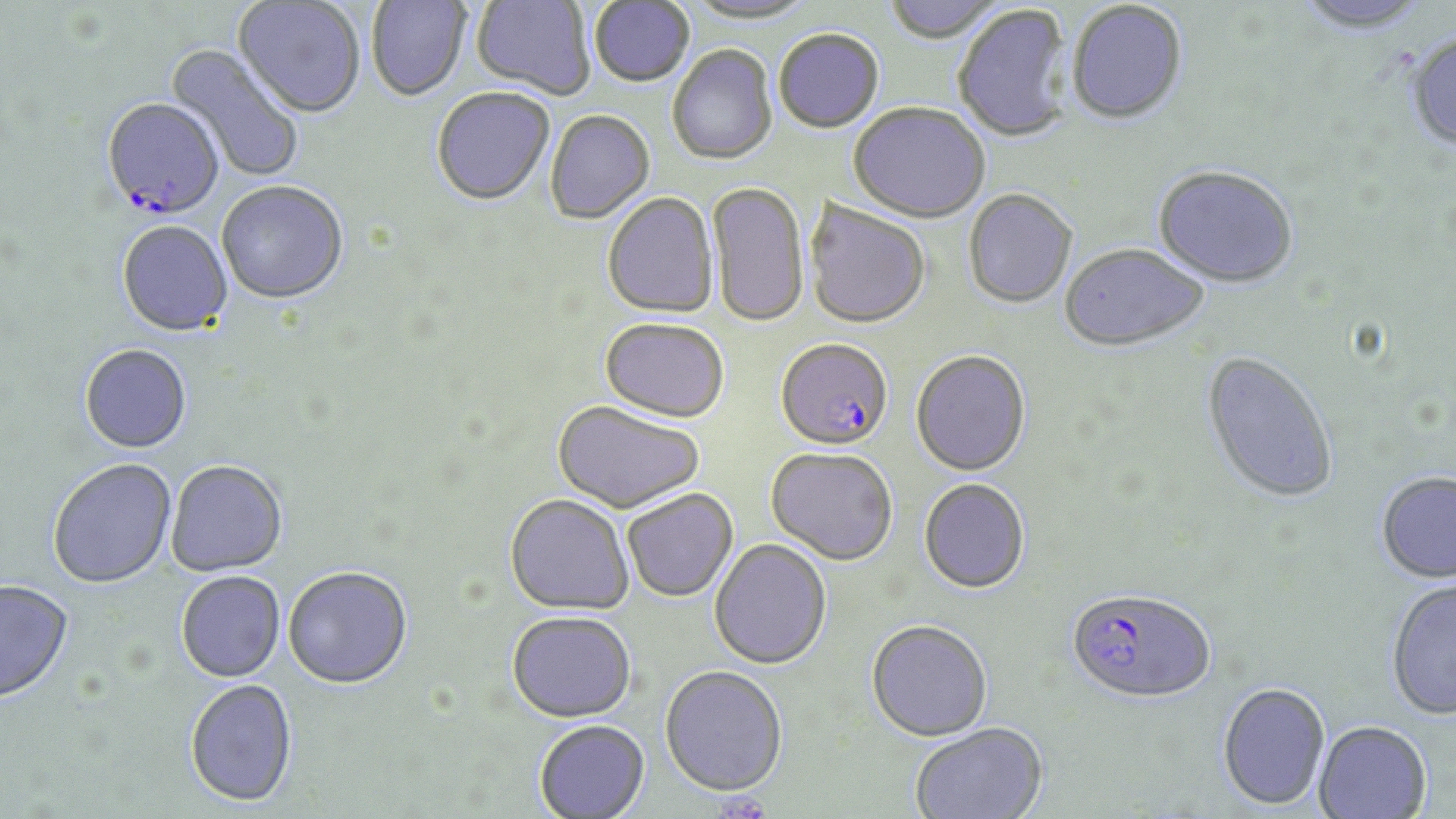
Approximate bounding boxes as (x1, y1, x2, y2) in pixels. Uninfected red blood cell locations: (233, 0, 366, 119), (366, 0, 471, 102), (682, 0, 819, 26), (881, 0, 1008, 46), (472, 1, 594, 100), (1292, 1, 1434, 37), (589, 2, 694, 88), (1067, 2, 1188, 127), (953, 5, 1075, 144), (773, 30, 884, 134), (1405, 32, 1456, 153), (166, 42, 304, 183), (668, 45, 778, 166), (432, 88, 555, 207), (848, 103, 989, 225), (545, 110, 654, 225), (1152, 166, 1298, 290), (706, 181, 809, 329), (216, 182, 349, 306), (963, 190, 1078, 309), (602, 193, 719, 319), (803, 199, 931, 330), (116, 222, 233, 338), (1060, 244, 1209, 353), (600, 318, 728, 424), (80, 345, 192, 454), (910, 351, 1031, 476), (1200, 352, 1339, 505), (551, 401, 706, 514), (766, 447, 898, 566), (47, 458, 177, 589), (165, 460, 288, 577), (1376, 472, 1456, 584), (919, 478, 1030, 594), (622, 489, 738, 602), (505, 494, 634, 615), (709, 538, 832, 670), (283, 567, 413, 689), (176, 571, 285, 682), (1385, 579, 1456, 720), (1, 580, 74, 703), (506, 610, 636, 722), (865, 619, 993, 741), (659, 665, 788, 797), (185, 679, 298, 807), (1217, 682, 1331, 811), (533, 719, 650, 818), (909, 721, 1049, 819), (1313, 722, 1432, 818). Plasmodium falciparum-infected red blood cell locations: (101, 100, 224, 221), (775, 338, 893, 453), (1065, 587, 1217, 703). Slide-level diagnosis: Plasmodium falciparum. Single field of view. Light microscopy. May-Grünwald-Giemsa-stained preparation. Image is 1456×819 pixels. 1000x magnification. Thin blood smear.